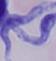
Summary:
  - Identification: trypanosome
  - Magnification: 1000x
  - Modality: micrograph